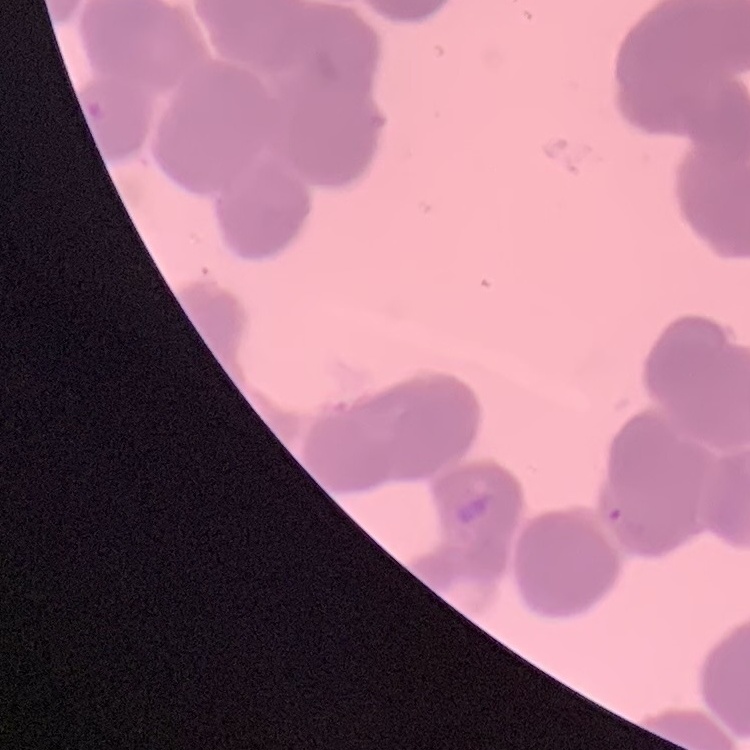
The erythrocytes exhibit rouleaux formation. Field's or Giemsa stain. Thin blood smear. One tile cut from a larger photomicrograph.